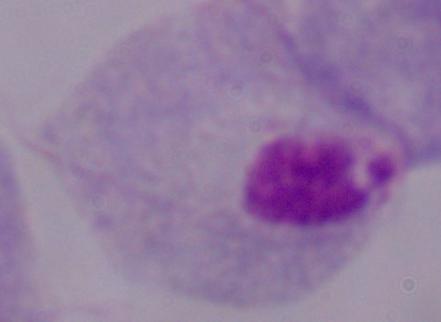

identification = trichomonad
magnification = 1000x
modality = micrograph